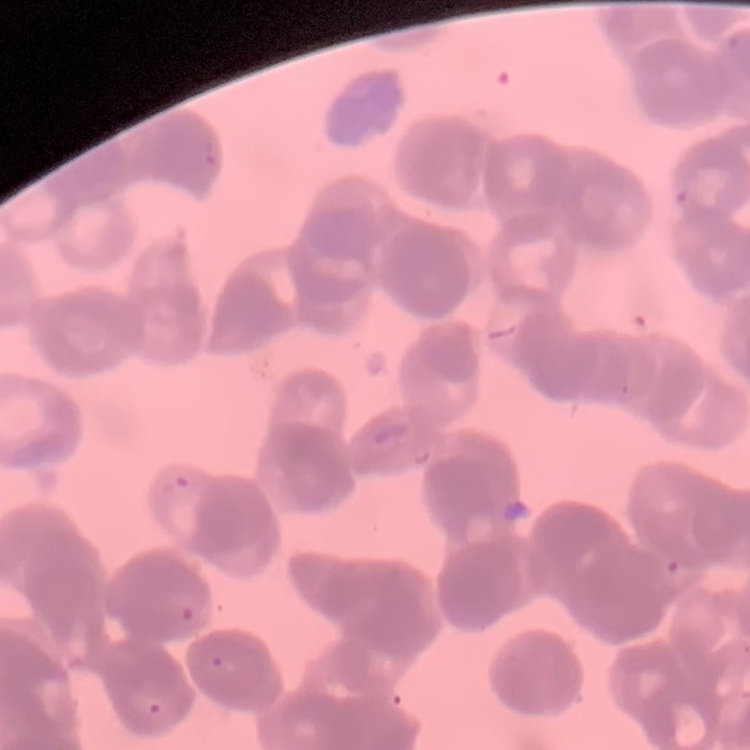
Summary:
  - Erythrocyte morphology: rouleaux formation
  - Stain: Field's or Giemsa
  - Image type: square crop of a larger photomicrograph
  - Preparation: thin peripheral smear